Give the extent of all Plasmodium ovale-infected red blood cells.
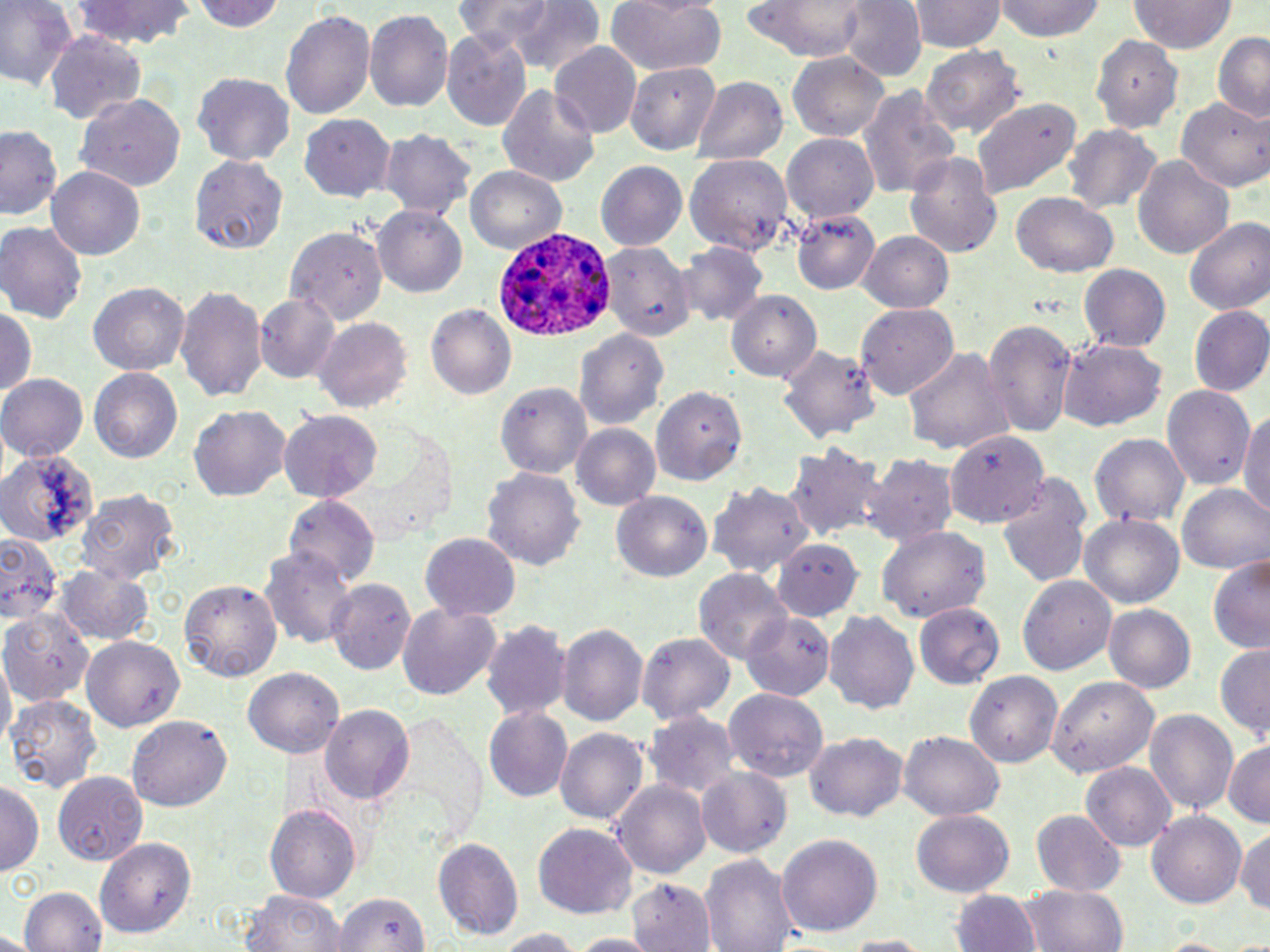

Approximate bounding boxes as (x1,y1)-(x2,y2) corner pairs in pixels.
Plasmodium ovale-infected red blood cells: (493,226)-(621,344).

Summary:
  - Uninfected red blood cell locations: (0,0)-(78,90), (67,0)-(198,50), (195,0)-(289,33), (449,0)-(578,61), (508,0)-(605,76), (605,0)-(727,76), (836,0)-(926,80), (993,0)-(1107,43), (742,1)-(871,58), (909,1)-(1003,54), (1129,1)-(1235,54), (280,8)-(375,120), (365,9)-(452,116), (440,29)-(531,130), (1213,30)-(1269,122), (42,32)-(145,124), (1094,32)-(1183,135), (549,42)-(641,140), (922,44)-(1022,139), (788,52)-(890,142), (621,64)-(721,150), (193,71)-(295,164), (695,77)-(786,165), (497,82)-(600,191), (858,86)-(960,201), (75,93)-(186,190), (970,97)-(1080,199), (1177,99)-(1266,191), (299,114)-(396,202), (0,125)-(62,224), (1067,125)-(1163,218), (377,131)-(475,222), (783,131)-(880,222), (903,150)-(1004,258), (684,154)-(794,251), (190,155)-(289,251), (1132,155)-(1235,259), (596,159)-(688,247), (46,166)-(148,260), (465,167)-(567,255), (1012,194)-(1117,276), (374,204)-(468,299), (792,207)-(880,294), (1185,216)-(1270,318), (0,221)-(87,324), (282,222)-(389,327), (859,233)-(954,311), (678,241)-(766,329), (600,242)-(693,341), (1080,264)-(1170,353), (88,283)-(190,376), (177,286)-(268,405), (727,291)-(819,383), (255,295)-(338,382), (424,302)-(516,402), (857,303)-(962,398), (0,304)-(35,406), (1188,305)-(1270,396), (982,319)-(1077,438), (314,321)-(411,410), (575,327)-(669,429), (1058,339)-(1167,432), (777,343)-(877,445), (903,345)-(1013,456), (90,368)-(182,464), (0,374)-(87,463), (496,379)-(593,477), (653,385)-(751,485), (1163,385)-(1253,495), (191,406)-(291,502), (280,413)-(381,503), (1240,413)-(1270,523), (572,424)-(660,511), (945,431)-(1049,526), (1091,431)-(1190,531), (785,446)-(884,542), (0,448)-(91,549), (862,455)-(958,545), (483,466)-(584,575), (996,475)-(1091,591), (709,479)-(816,582), (1177,484)-(1269,573), (76,488)-(181,587), (612,491)-(713,583), (286,496)-(379,587), (1080,514)-(1184,609), (879,525)-(992,622), (1,533)-(65,628), (421,534)-(520,621), (772,540)-(862,621), (262,546)-(359,651), (1206,555)-(1270,654), (56,566)-(156,645), (693,569)-(791,665), (1019,574)-(1116,675), (180,577)-(282,683), (328,578)-(414,674), (1103,601)-(1196,692), (397,603)-(501,699), (915,605)-(1002,689), (823,610)-(918,713), (5,613)-(98,700), (743,613)-(832,699), (483,619)-(570,722), (558,622)-(649,728), (638,634)-(735,724), (80,637)-(183,732), (1214,645)-(1270,738), (243,668)-(344,756), (964,669)-(1063,767), (1046,675)-(1157,777), (724,687)-(828,781), (7,694)-(101,796), (322,705)-(414,804), (1144,707)-(1237,816), (484,708)-(570,798), (382,710)-(487,842), (645,710)-(737,800), (129,716)-(233,811), (554,729)-(649,825), (804,733)-(909,821), (900,733)-(1003,819), (1221,742)-(1270,826), (1083,762)-(1177,850), (52,769)-(144,865), (696,771)-(791,858), (613,778)-(710,880), (0,782)-(43,875), (265,805)-(361,903), (911,810)-(1012,897), (1029,810)-(1126,895), (1147,811)-(1246,906), (1236,822)-(1270,915), (534,826)-(637,916), (775,834)-(883,939), (97,837)-(197,938), (431,837)-(525,940), (700,854)-(799,952), (626,875)-(716,950), (19,883)-(107,951), (1020,884)-(1128,952), (241,889)-(347,952), (952,889)-(1039,952), (333,891)-(429,952), (486,928)-(586,950), (567,932)-(659,952), (835,934)-(936,951)
  - Slide-level diagnosis: Plasmodium ovale
  - Image size: 1270×952 pixels
  - Magnification: 1000x
  - Stain: May-Grünwald-Giemsa
  - Modality: light microscopy
  - Preparation: thin blood smear
  - Field of view: single